Name the cell type shown.
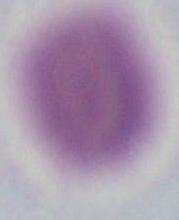

An erythrocyte.

Captured at 1000x magnification. Photomicrograph.